Report the malaria status of this cell.
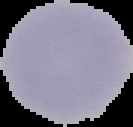
Uninfected.

preparation = thin blood film
image size = 133×127 pixels
image type = segmented cell region on a black background